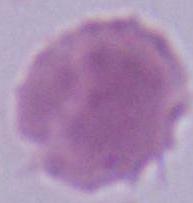

magnification = 1000x
identification = erythrocyte
modality = micrograph